Classify this cell by malaria status.
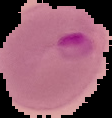

It is parasitized.

image type = segmented cell region on a black background
image size = 112×118 pixels
preparation = thin blood smear